Assess the morphology of the erythrocytes.
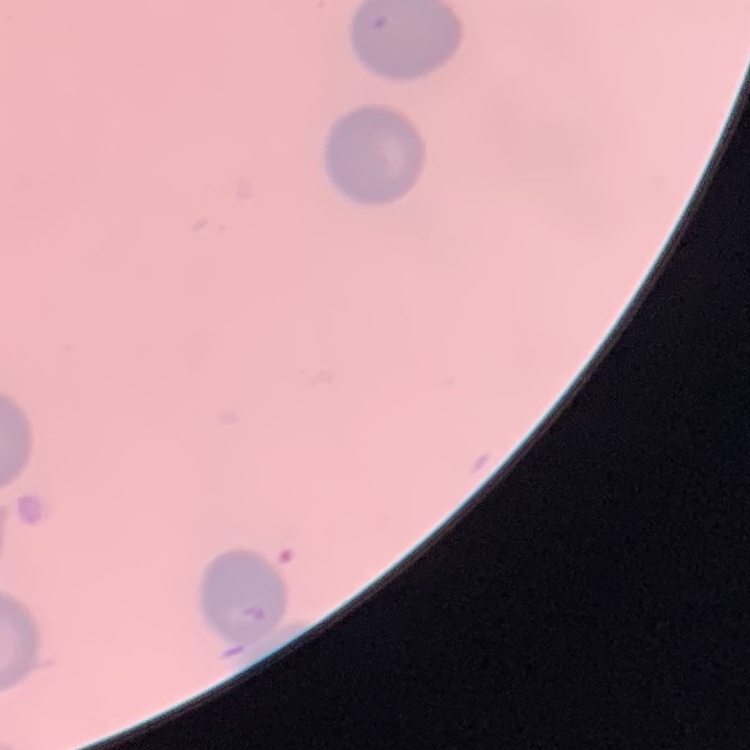
They show no rouleaux formation.

Thin blood film. One tile cut from a larger photomicrograph. Stained with either Field's or Giemsa.